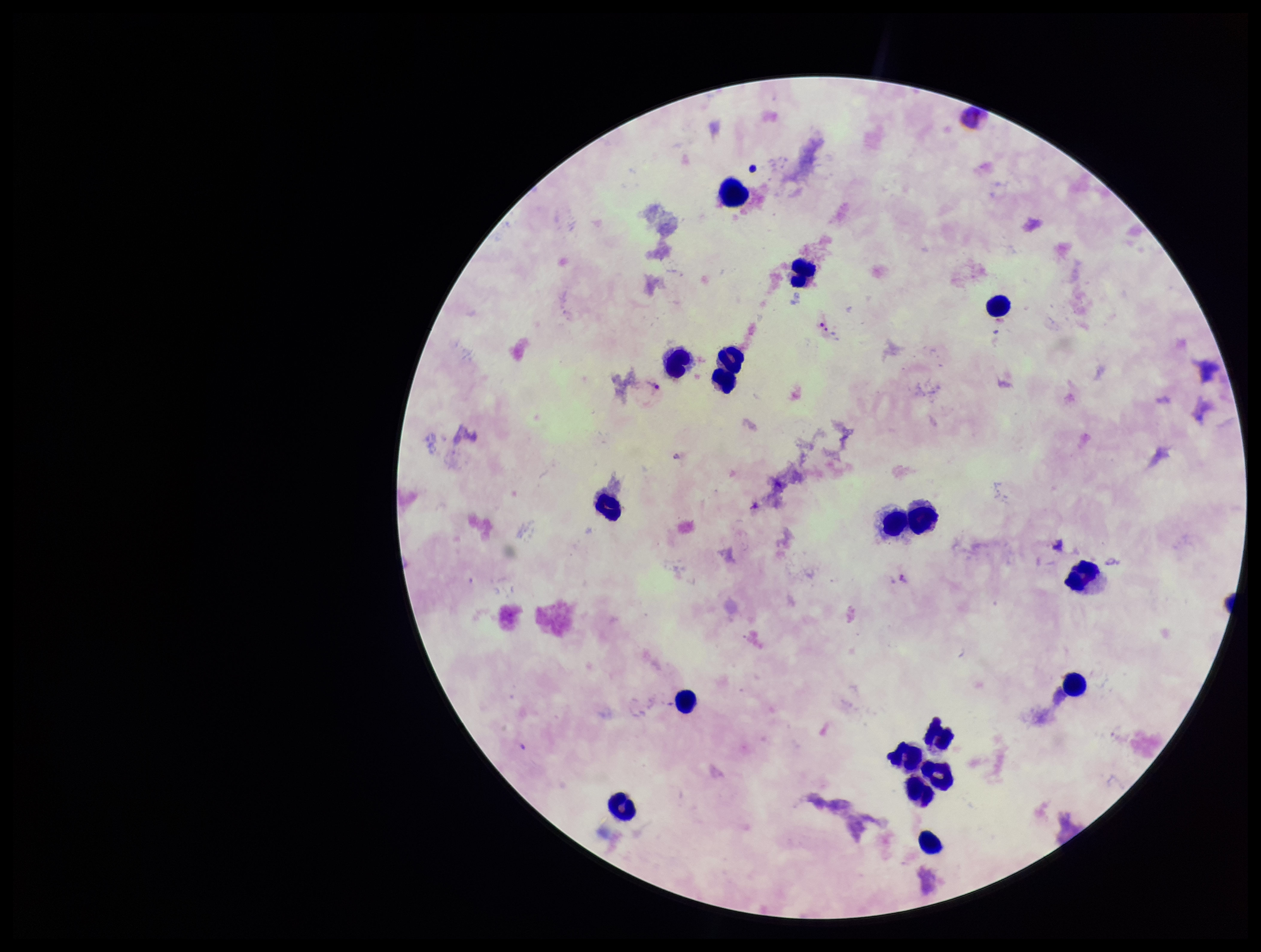

capture = smartphone photograph through the microscope eyepiece
stain = Giemsa
Plasmodium parasites = detected
parasite count = 4
image size = 1261×952 pixels
patient malaria status = infected
species reported for this patient = Plasmodium vivax
leukocyte count = 18
field of view = one from this slide
preparation = thick smear